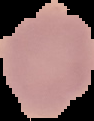
image_size: 94×121 pixels
image_type: cell region segmented out of the field of view; surrounding area masked to black
preparation: thin blood film
malaria_status: uninfected